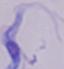
magnification = 1000x
identification = trypanosome
modality = photomicrograph